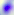

{
  "modality": "photomicrograph",
  "identification": "Toxoplasma gondii",
  "magnification": "400x"
}